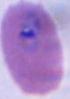

Summary:
  - Modality: micrograph
  - Magnification: 400x or 1000x
  - Identification: Plasmodium